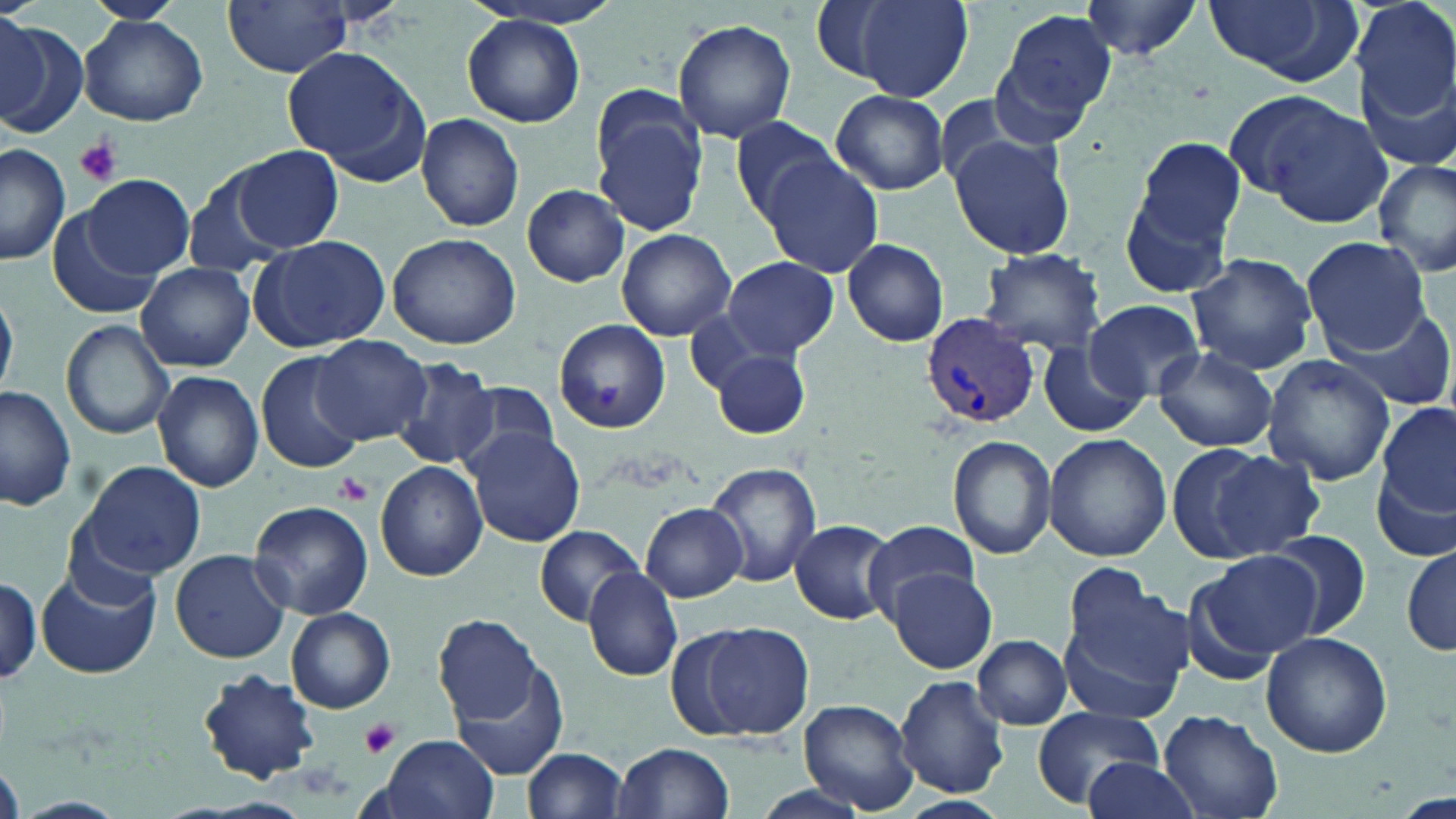

Summary:
  - Coordinate format: approximate bounding boxes as (x1, y1, x2, y2) in pixels
  - Platelet locations: (73, 137, 122, 186), (333, 471, 373, 506), (359, 719, 402, 760)
  - Plasmodium vivax-infected red blood cell locations: (919, 313, 1040, 429)
  - Uninfected red blood cell locations: (86, 0, 182, 24), (468, 0, 634, 29), (1078, 0, 1206, 59), (1201, 0, 1362, 87), (1352, 0, 1456, 128), (223, 1, 354, 77), (825, 1, 973, 100), (997, 7, 1119, 126), (79, 15, 208, 126), (0, 16, 47, 122), (463, 16, 586, 126), (671, 20, 796, 140), (0, 21, 86, 140), (282, 47, 425, 174), (1360, 72, 1456, 178), (831, 89, 950, 195), (1251, 97, 1396, 227), (591, 107, 706, 238), (416, 112, 524, 232), (728, 115, 847, 226), (949, 133, 1077, 260), (1136, 138, 1246, 247), (0, 145, 70, 266), (234, 146, 344, 252), (758, 155, 884, 279), (1374, 158, 1456, 277), (185, 168, 293, 279), (1116, 170, 1238, 302), (83, 175, 195, 279), (523, 185, 630, 287), (49, 213, 164, 320), (616, 229, 735, 342), (388, 232, 520, 350), (251, 235, 389, 350), (1300, 236, 1431, 354), (842, 238, 949, 347), (978, 250, 1106, 354), (1186, 252, 1317, 375), (721, 256, 839, 358), (136, 262, 255, 372), (0, 289, 18, 398), (1085, 299, 1204, 399), (1325, 301, 1455, 413), (685, 312, 796, 407), (554, 319, 670, 433), (62, 320, 174, 441), (105, 323, 234, 485), (312, 335, 433, 446), (1038, 341, 1148, 438), (1153, 346, 1278, 452), (713, 349, 810, 440), (258, 352, 368, 478), (1261, 355, 1393, 486), (393, 359, 501, 471), (152, 370, 262, 492), (450, 381, 562, 481), (0, 385, 76, 513), (1378, 401, 1456, 522), (463, 425, 585, 547), (1042, 432, 1171, 562), (948, 434, 1057, 560), (1191, 444, 1322, 561), (71, 461, 210, 582), (704, 461, 819, 587), (375, 462, 486, 581), (1376, 471, 1454, 565), (249, 500, 373, 619), (642, 500, 748, 601), (789, 518, 897, 626), (865, 519, 981, 622), (534, 524, 644, 627), (1262, 530, 1372, 641), (1400, 545, 1455, 658), (170, 549, 289, 663), (1193, 550, 1321, 666), (1060, 565, 1192, 703), (38, 566, 159, 679), (581, 566, 682, 682), (887, 569, 996, 672), (0, 575, 42, 685), (286, 608, 396, 713), (432, 615, 545, 723), (698, 622, 816, 738), (1260, 632, 1393, 758), (973, 635, 1071, 730), (450, 655, 571, 779), (198, 668, 322, 783), (894, 675, 1010, 797), (798, 698, 920, 815), (1030, 705, 1164, 810), (1159, 707, 1284, 819), (374, 734, 498, 819), (611, 742, 735, 819), (522, 747, 630, 819), (1083, 757, 1199, 818), (746, 785, 875, 819), (895, 796, 1012, 819)
  - Slide-level diagnosis: Plasmodium vivax
  - Stain: May-Grünwald-Giemsa
  - Magnification: 1000x
  - Modality: optical microscopy
  - Image size: 1456×819 pixels
  - Field of view: one of a larger specimen
  - Preparation: thin blood film